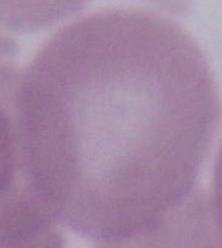
Summary:
  - Identification: erythrocyte
  - Modality: micrograph
  - Magnification: 1000x